Assess the morphology of the red blood cells.
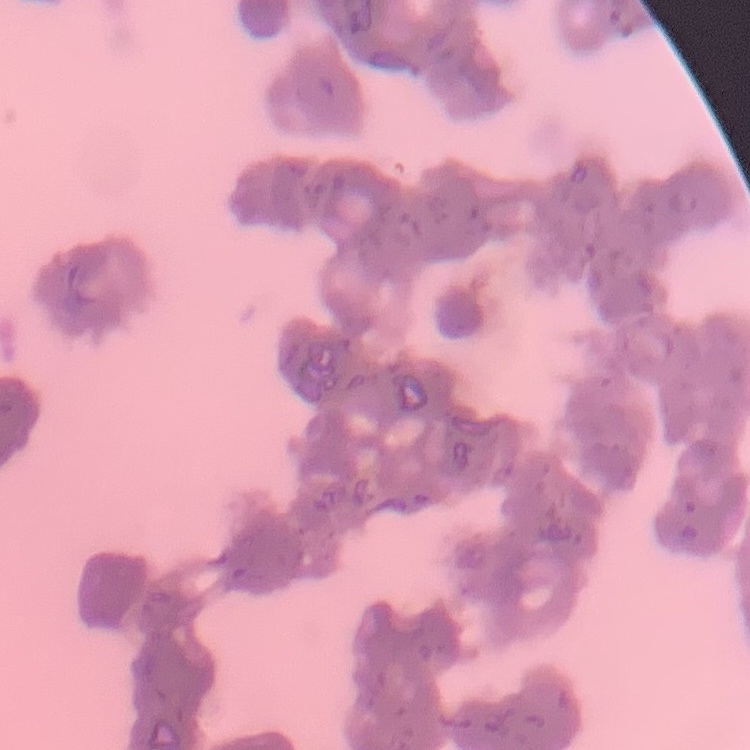
Rouleaux formation.

Summary:
  - Stain: Field's or Giemsa
  - Image type: square crop of a larger photomicrograph
  - Preparation: thin blood film